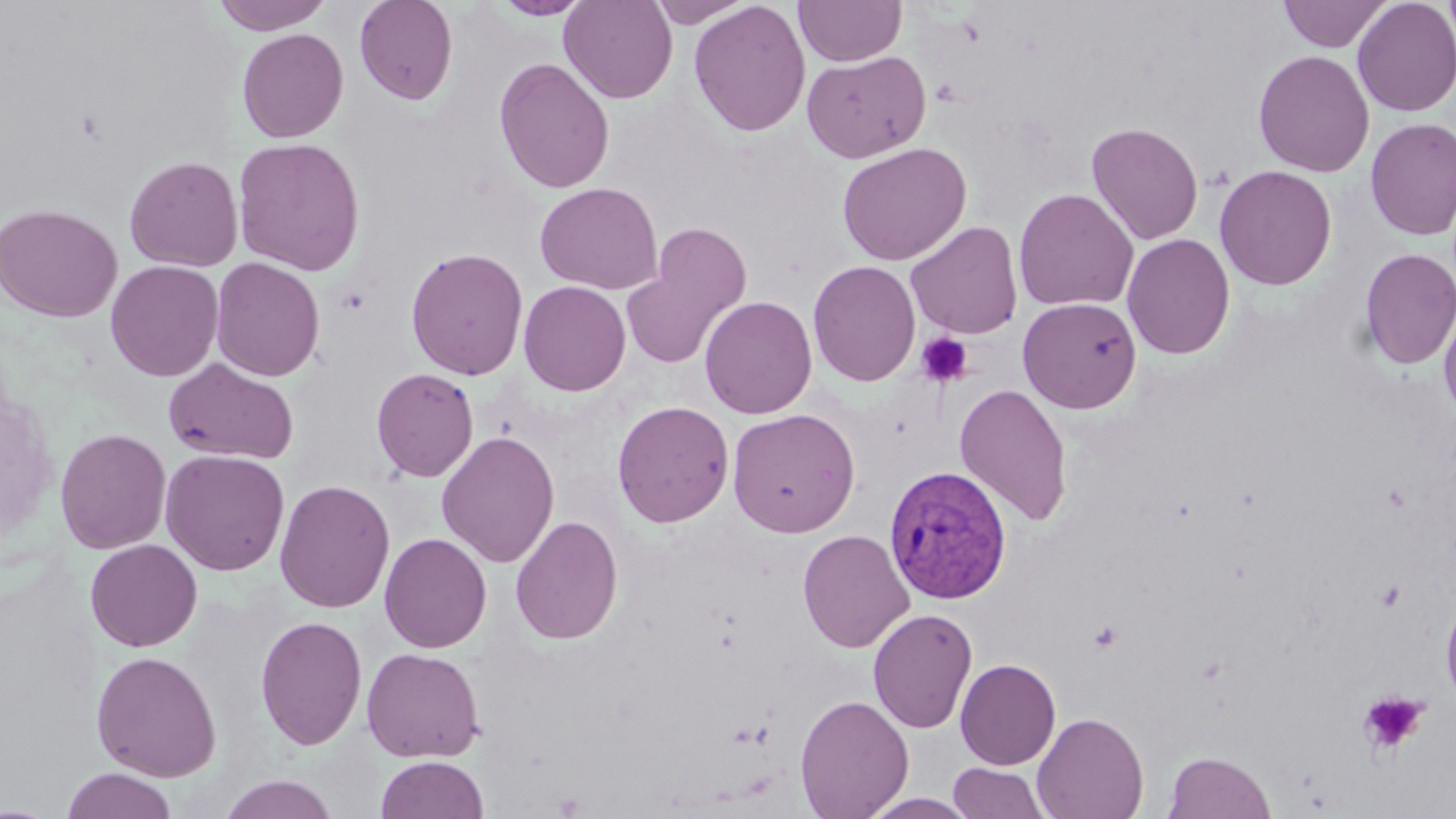
Summary:
  - Coordinate format: approximate bounding boxes as (x1, y1, x2, y2) in pixels
  - Plasmodium vivax-infected red blood cell locations: (884, 463, 1013, 606)
  - Platelet locations: (916, 332, 974, 387), (1374, 579, 1407, 612), (1357, 690, 1429, 757)
  - Uninfected red blood cell locations: (211, 0, 334, 35), (354, 0, 458, 105), (492, 0, 593, 20), (559, 0, 677, 103), (647, 0, 753, 27), (688, 0, 811, 138), (794, 0, 907, 66), (1277, 0, 1393, 52), (1352, 0, 1456, 117), (1442, 0, 1456, 49), (237, 27, 349, 143), (1253, 49, 1375, 177), (802, 50, 931, 164), (494, 57, 615, 193), (1365, 117, 1456, 240), (1085, 121, 1204, 246), (232, 136, 366, 276), (836, 141, 972, 266), (124, 155, 244, 272), (1214, 165, 1338, 290), (534, 182, 662, 295), (1013, 187, 1139, 312), (0, 202, 123, 323), (905, 220, 1023, 339), (622, 223, 753, 370), (1121, 232, 1236, 360), (405, 247, 529, 381), (1359, 247, 1456, 370), (209, 257, 325, 381), (105, 260, 224, 381), (807, 260, 921, 386), (518, 281, 631, 396), (699, 295, 818, 419), (1018, 297, 1142, 414), (1439, 297, 1456, 425), (163, 358, 299, 465), (371, 368, 479, 482), (954, 383, 1073, 526), (612, 401, 734, 527), (727, 407, 860, 538), (55, 427, 172, 555), (436, 430, 560, 568), (160, 449, 290, 576), (274, 479, 395, 613), (510, 514, 623, 645), (797, 529, 915, 653), (379, 532, 492, 653), (85, 538, 203, 652), (1439, 590, 1456, 711), (867, 607, 978, 734), (255, 615, 368, 750), (361, 646, 485, 762), (91, 650, 222, 781), (955, 658, 1061, 770), (795, 694, 913, 818), (1032, 711, 1149, 819), (1163, 750, 1276, 819), (376, 755, 490, 819), (947, 762, 1051, 818), (60, 767, 180, 819), (217, 774, 341, 818), (860, 792, 980, 819), (0, 803, 65, 818)
  - Slide-level diagnosis: Plasmodium vivax
  - Stain: May-Grünwald-Giemsa
  - Image size: 1456×819 pixels
  - Modality: optical microscopy
  - Magnification: 1000x
  - Preparation: thin blood film
  - Field of view: one of a larger specimen